Locate every uninfected red blood cell.
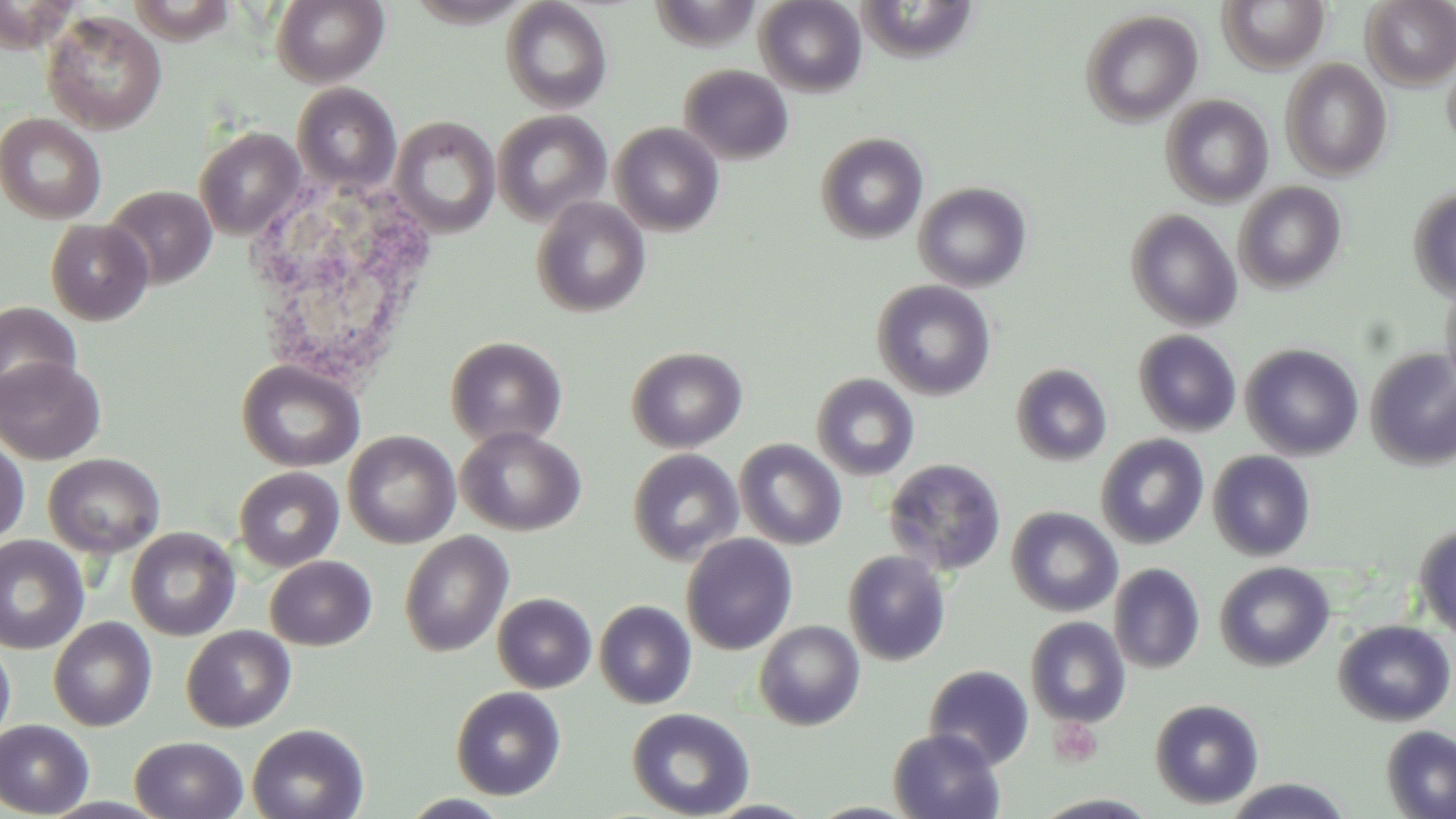
Approximate bounding boxes as [x1, y1, x2, y2] in pixels.
Uninfected red blood cells: [271, 0, 389, 87], [500, 0, 613, 113], [755, 0, 867, 96], [1361, 0, 1456, 89], [1219, 1, 1329, 72], [1080, 8, 1202, 126], [42, 10, 167, 134], [1442, 53, 1456, 154], [1280, 59, 1392, 180], [679, 64, 794, 165], [292, 82, 401, 195], [1161, 94, 1274, 207], [492, 110, 610, 225], [0, 113, 106, 224], [390, 116, 500, 237], [611, 123, 724, 236], [194, 126, 306, 239], [815, 131, 929, 244], [912, 181, 1033, 292], [1233, 181, 1347, 293], [104, 185, 217, 289], [1408, 187, 1456, 302], [531, 197, 651, 318], [1126, 208, 1242, 331], [45, 219, 154, 325], [872, 280, 996, 401], [1441, 280, 1456, 396], [0, 301, 82, 404], [1133, 329, 1242, 436], [446, 335, 567, 449], [1241, 343, 1364, 460], [626, 346, 747, 453], [1365, 348, 1456, 470], [0, 356, 106, 464], [237, 360, 365, 472], [1011, 363, 1112, 465], [811, 373, 920, 481], [456, 426, 586, 536], [343, 430, 460, 549], [1095, 433, 1209, 549], [734, 438, 847, 550], [0, 439, 29, 545], [627, 448, 743, 565], [1207, 450, 1316, 561], [44, 453, 165, 558], [884, 458, 1006, 576], [234, 466, 344, 572], [1006, 506, 1123, 617], [1414, 523, 1456, 642], [126, 527, 240, 641], [399, 531, 514, 656], [681, 533, 798, 655], [0, 535, 89, 654], [843, 550, 951, 666], [265, 555, 377, 650], [1214, 561, 1335, 671], [1109, 562, 1205, 674], [492, 592, 597, 693], [594, 599, 696, 709], [1025, 615, 1131, 728], [48, 617, 157, 731], [754, 620, 865, 730], [1333, 621, 1454, 726], [181, 625, 296, 732], [0, 637, 16, 749], [924, 664, 1035, 770], [451, 686, 566, 800], [1150, 698, 1265, 809], [626, 707, 755, 819], [0, 719, 94, 817], [247, 723, 369, 819], [1381, 725, 1456, 819], [889, 728, 1006, 819], [130, 735, 248, 819], [1218, 778, 1355, 819], [1031, 793, 1163, 818].

slide-level diagnosis = no evidence of blood parasites
magnification = 1000x
modality = light microscopy
field of view = single
preparation = thin blood film
white blood cell locations = approximate bounding boxes as [x1, y1, x2, y2] in pixels: [247, 171, 440, 396]
stain = May-Grünwald-Giemsa
image size = 1456×819 pixels